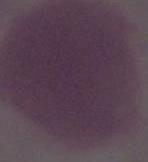

{
  "magnification": "1000x",
  "modality": "photomicrograph",
  "identification": "erythrocyte"
}